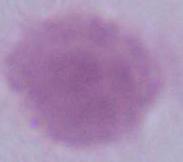
An erythrocyte is shown. Micrograph. 1000x magnification.